Describe the morphology of the red blood cells.
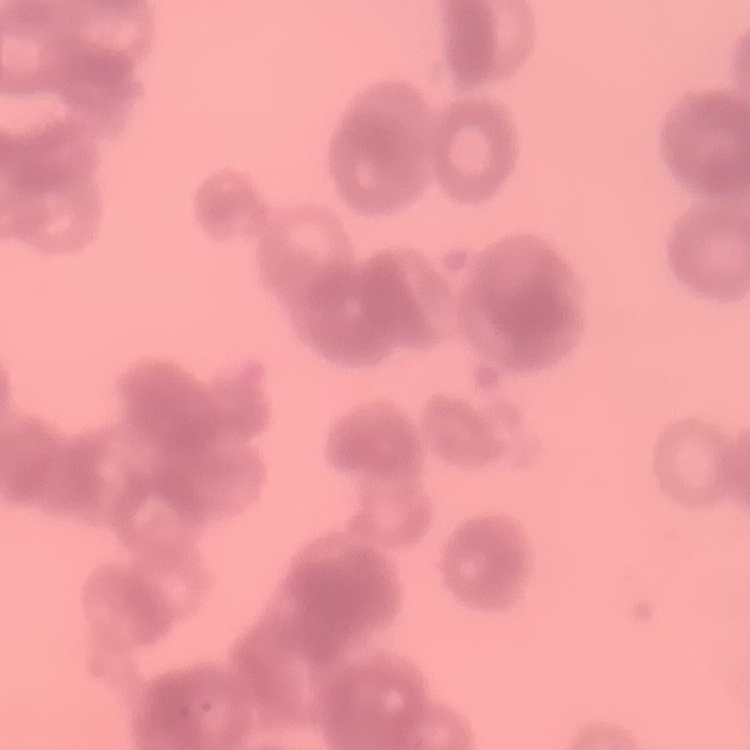

They show rouleaux formation.

stain: Field's or Giemsa
preparation: thin blood smear
image_type: square crop of a larger photomicrograph